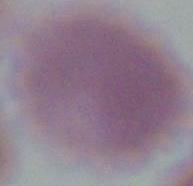
Summary:
  - Identification: red blood cell
  - Modality: photomicrograph
  - Magnification: 1000x